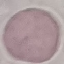

Malaria status: uninfected. Thin smear of blood. Photographed with a smartphone camera at the microscope eyepiece. Cell patch, automatically extracted from a larger field of view and resized to 64 × 64 pixels. Giemsa stain.